Identify the cell.
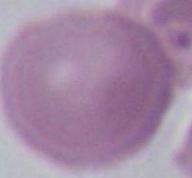
This is an erythrocyte.

1000x magnification. Photomicrograph.